Outline each blood parasite and name the species.
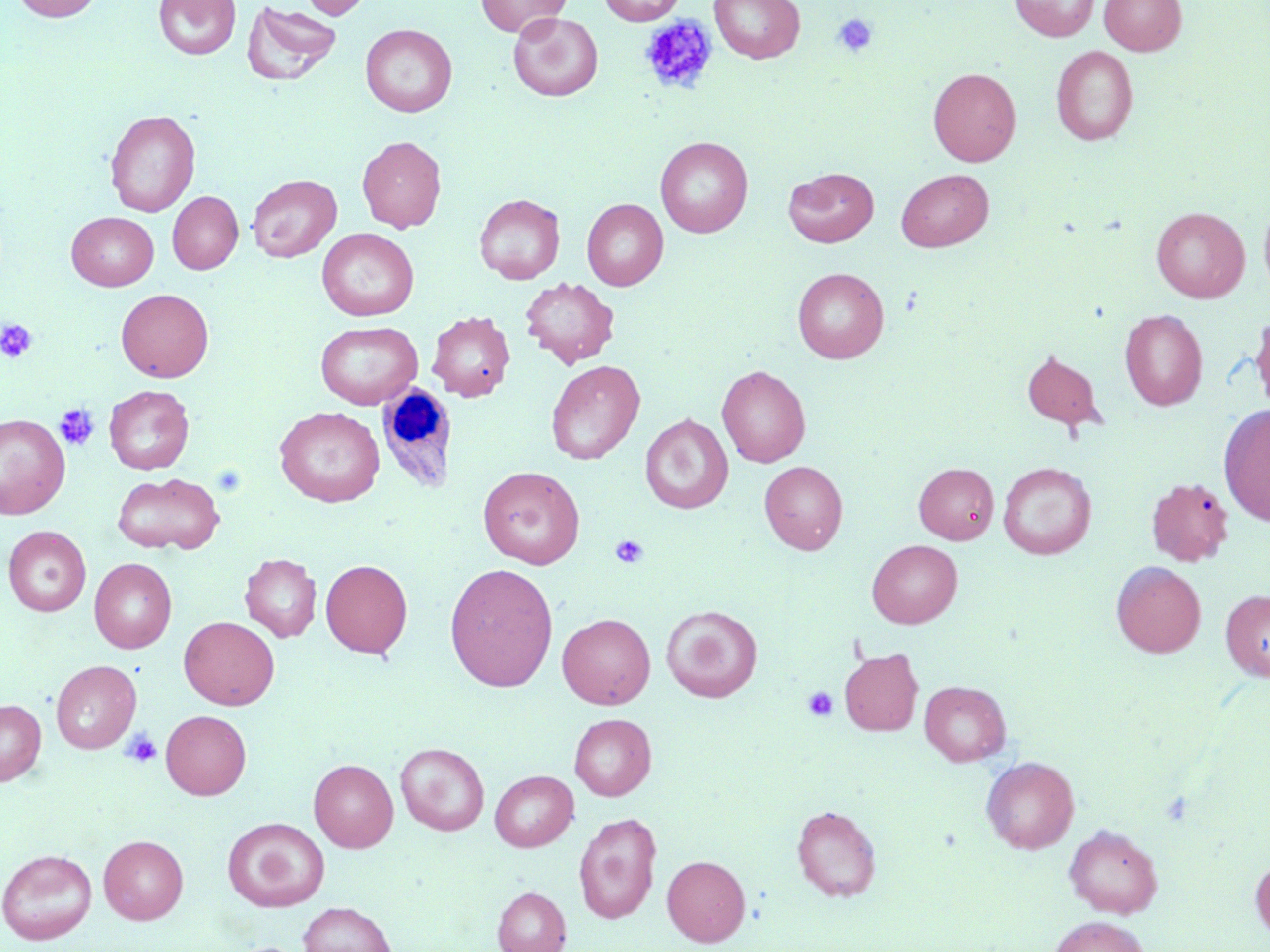

No blood parasites seen.

slide_level_diagnosis: negative for blood parasites
field_of_view: single
white_blood_cell_locations: 'approximate bounding boxes as [x1, y1, x2, y2] in pixels: [376, 382, 451, 493]'
image_size: 1270×952 pixels
uninfected_red_blood_cell_locations: 'approximate bounding boxes as [x1, y1, x2, y2] in pixels: [12, 0, 103, 22], [154, 0, 241, 60], [299, 0, 372, 19], [598, 0, 685, 25], [710, 0, 805, 63], [1010, 0, 1100, 41], [1099, 0, 1186, 55], [476, 1, 569, 38], [242, 2, 342, 85], [508, 12, 603, 101], [360, 23, 457, 117], [1052, 46, 1138, 146], [928, 67, 1021, 166], [105, 109, 200, 217], [357, 135, 446, 233], [655, 136, 753, 238], [783, 167, 879, 247], [896, 169, 994, 252], [247, 174, 341, 262], [168, 191, 242, 274], [474, 194, 565, 284], [582, 198, 668, 290], [1259, 199, 1270, 301], [1151, 206, 1249, 302], [67, 212, 158, 291], [317, 228, 419, 321], [792, 267, 888, 363], [519, 277, 619, 369], [116, 289, 214, 382], [1119, 309, 1207, 410], [427, 311, 515, 401], [1250, 313, 1270, 417], [315, 321, 422, 409], [1022, 349, 1104, 429], [546, 360, 645, 465], [717, 364, 811, 467], [103, 385, 194, 473], [1219, 403, 1270, 527], [274, 406, 384, 507], [0, 414, 70, 519], [640, 414, 733, 514], [760, 461, 848, 555], [998, 462, 1096, 559], [914, 463, 999, 543], [478, 465, 585, 568], [112, 473, 224, 554], [1146, 477, 1233, 566], [3, 526, 91, 616], [867, 540, 963, 628], [240, 553, 321, 642], [89, 558, 176, 652], [321, 559, 413, 658], [1111, 561, 1206, 658], [445, 563, 558, 691], [1220, 589, 1270, 681], [661, 604, 763, 702], [557, 613, 656, 708], [179, 616, 279, 710], [839, 647, 923, 736], [51, 660, 141, 753], [920, 680, 1011, 766], [0, 698, 46, 785], [161, 710, 251, 799], [569, 713, 656, 801], [395, 742, 489, 835], [980, 756, 1080, 853], [309, 759, 399, 852], [489, 770, 578, 851], [791, 805, 881, 902], [574, 813, 662, 924], [223, 817, 330, 912], [1064, 824, 1163, 918], [99, 835, 189, 924], [0, 849, 97, 944], [662, 855, 750, 946], [1250, 856, 1270, 942], [492, 886, 571, 952], [297, 902, 397, 952], [1050, 915, 1149, 952]'
modality: optical microscopy
stain: May-Grünwald-Giemsa
magnification: 1000x
platelet_locations: 'approximate bounding boxes as [x1, y1, x2, y2] in pixels: [833, 13, 878, 57], [638, 14, 718, 95], [0, 319, 37, 363], [55, 404, 100, 451], [610, 534, 649, 569], [802, 686, 838, 722], [122, 729, 162, 768]'
preparation: thin blood film